Classify this cell by malaria status.
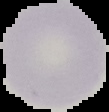
It is uninfected.

preparation = thin blood smear
image type = segmented cell region on a black background
image size = 109×112 pixels